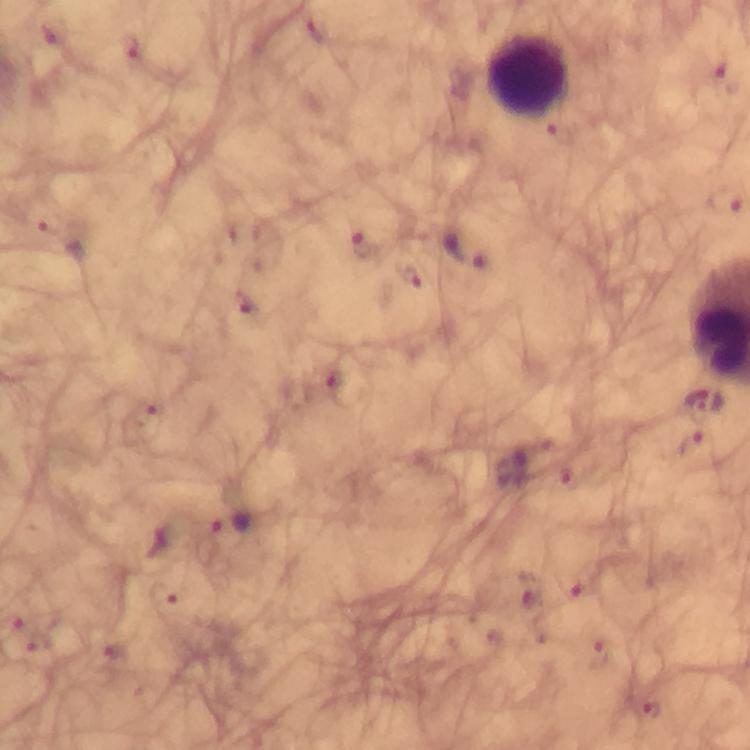 Approximate centers as (x, y) in pixels. Leukocyte locations: (528, 77). Malaria parasite locations: (319, 30), (132, 50), (727, 78), (723, 200), (47, 223), (363, 245), (465, 249), (411, 277), (248, 304), (701, 401), (696, 445), (229, 527), (575, 586), (531, 589), (650, 710). Cropped region of a single field of view. Image is 750×750 pixels. 100x magnification. Giemsa-stained preparation. Immersion oil was used. Smartphone photograph taken through a microscope. From a diagnostic examination for malaria. Thick blood smear.